Comment on the morphology of the red blood cells.
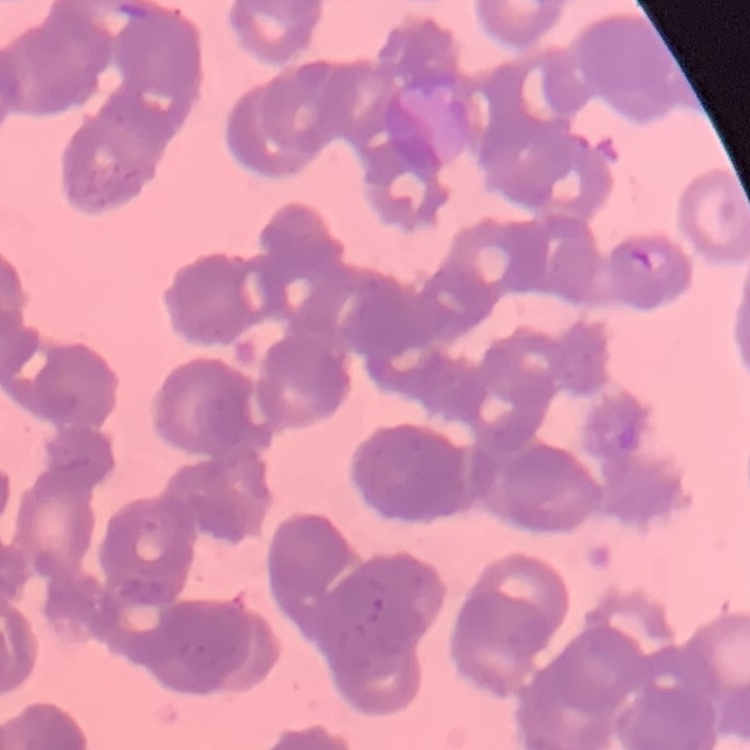

Rouleaux formation.

Stained with either Field's or Giemsa. One tile cut from a larger photomicrograph. Thin blood film.